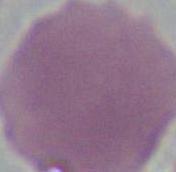

{
  "identification": "erythrocyte",
  "modality": "photomicrograph",
  "magnification": "1000x"
}